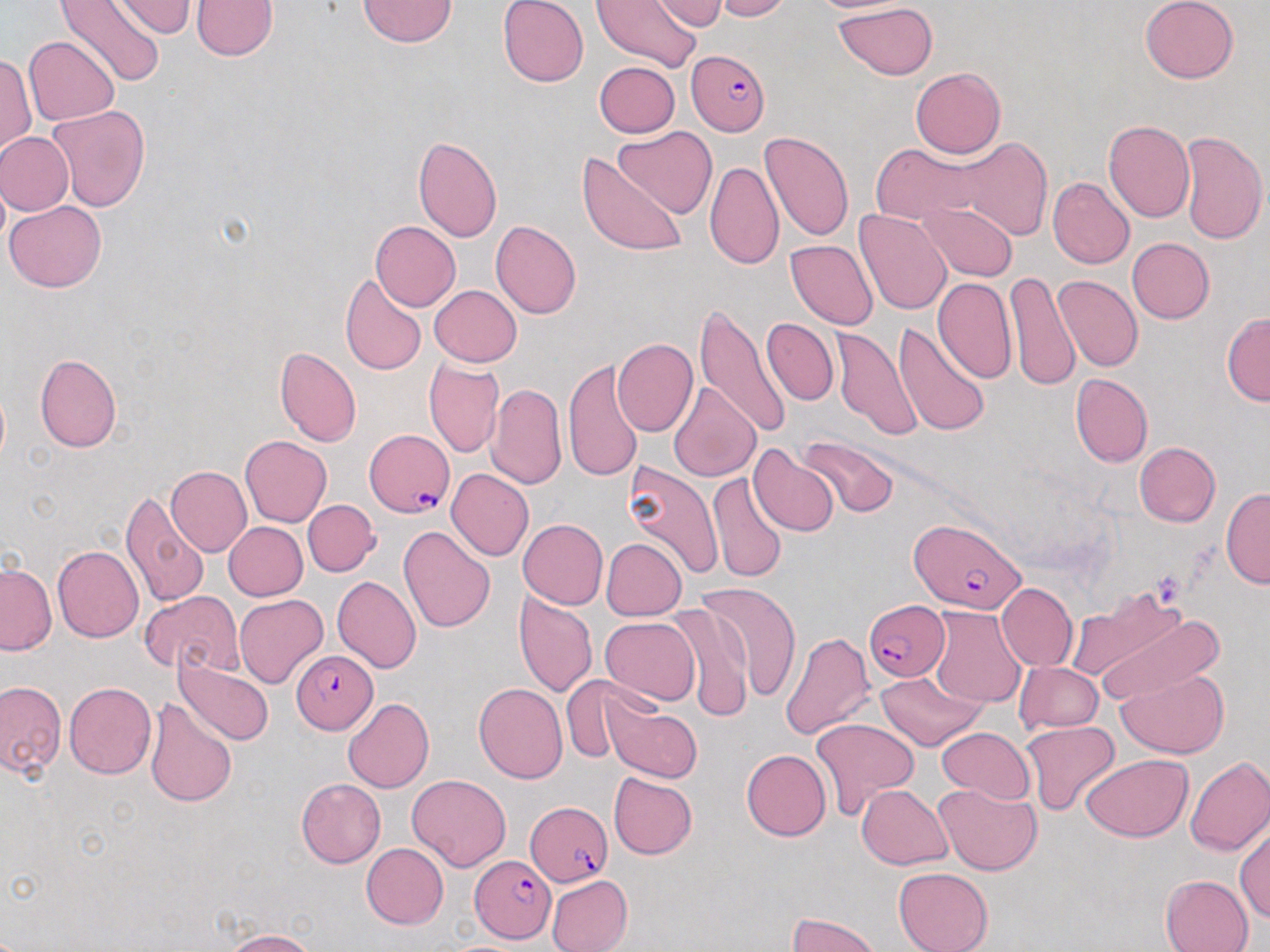

{
  "plasmodium_falciparum_infected_red_blood_cell_locations": "approximate bounding boxes as [x1, y1, x2, y2] in pixels: [686, 48, 769, 135], [365, 429, 454, 516], [910, 519, 1027, 613], [864, 600, 945, 682], [291, 649, 379, 734], [524, 800, 613, 890], [470, 855, 556, 943]",
  "slide_level_diagnosis": "Plasmodium falciparum",
  "image_size": "1270×952 pixels",
  "stain": "May-Grünwald-Giemsa",
  "magnification": "1000x",
  "field_of_view": "single",
  "preparation": "thin blood smear",
  "modality": "light microscopy",
  "uninfected_red_blood_cell_locations": "approximate bounding boxes as [x1, y1, x2, y2] in pixels: [55, 0, 164, 90], [192, 0, 279, 60], [358, 0, 458, 48], [497, 0, 589, 86], [592, 0, 699, 73], [712, 0, 792, 21], [805, 0, 923, 16], [1140, 0, 1240, 84], [112, 1, 199, 38], [651, 2, 733, 32], [833, 2, 938, 81], [24, 36, 119, 125], [1, 53, 36, 155], [594, 61, 681, 137], [910, 66, 1004, 158], [46, 104, 151, 212], [1104, 120, 1195, 222], [612, 126, 718, 218], [1179, 130, 1267, 244], [0, 131, 74, 215], [760, 132, 853, 242], [413, 136, 502, 242], [952, 138, 1052, 242], [871, 143, 987, 225], [578, 151, 688, 257], [705, 159, 783, 271], [1047, 177, 1135, 270], [5, 200, 107, 293], [919, 202, 1018, 281], [851, 208, 952, 314], [491, 220, 581, 319], [370, 221, 460, 311], [1126, 238, 1215, 324], [786, 240, 878, 330], [1004, 269, 1080, 394], [339, 273, 427, 375], [1054, 274, 1143, 372], [932, 277, 1016, 382], [430, 285, 522, 367], [693, 301, 791, 443], [1221, 311, 1270, 407], [762, 318, 838, 406], [893, 321, 991, 437], [832, 327, 923, 441], [612, 338, 698, 436], [274, 347, 362, 447], [35, 354, 122, 452], [424, 357, 504, 458], [562, 357, 645, 483], [426, 369, 566, 475], [1071, 373, 1153, 467], [670, 382, 761, 482], [487, 383, 568, 491], [240, 434, 332, 527], [799, 435, 897, 517], [1134, 441, 1221, 526], [749, 445, 840, 536], [166, 466, 252, 557], [623, 466, 743, 579], [446, 468, 533, 560], [707, 473, 787, 583], [1220, 487, 1270, 589], [120, 490, 210, 609], [303, 499, 380, 576], [518, 519, 608, 609], [224, 522, 307, 600], [399, 524, 496, 632], [600, 537, 687, 621], [53, 545, 144, 642], [0, 562, 56, 655], [332, 574, 421, 673], [698, 581, 802, 701], [996, 582, 1077, 671], [141, 591, 242, 676], [513, 591, 598, 698], [234, 593, 329, 689], [668, 603, 753, 724], [928, 607, 1026, 709], [1087, 609, 1220, 706], [599, 616, 700, 706], [780, 632, 875, 740], [174, 655, 275, 747], [1014, 661, 1103, 734], [1116, 668, 1230, 759], [877, 671, 985, 750], [561, 677, 641, 765], [0, 680, 66, 777], [64, 682, 156, 778], [474, 683, 567, 784], [599, 693, 703, 783], [146, 697, 238, 807], [343, 698, 433, 793], [810, 717, 919, 818], [1020, 720, 1121, 815], [936, 726, 1034, 805], [742, 749, 832, 841], [1081, 755, 1193, 842], [1183, 755, 1270, 856], [607, 772, 698, 860], [407, 774, 511, 871], [296, 777, 385, 868], [933, 782, 1042, 876], [856, 784, 952, 868], [1235, 822, 1269, 924], [361, 843, 448, 929], [893, 867, 994, 952], [1160, 874, 1254, 952], [546, 875, 633, 952], [786, 912, 883, 952], [223, 929, 316, 951]"
}